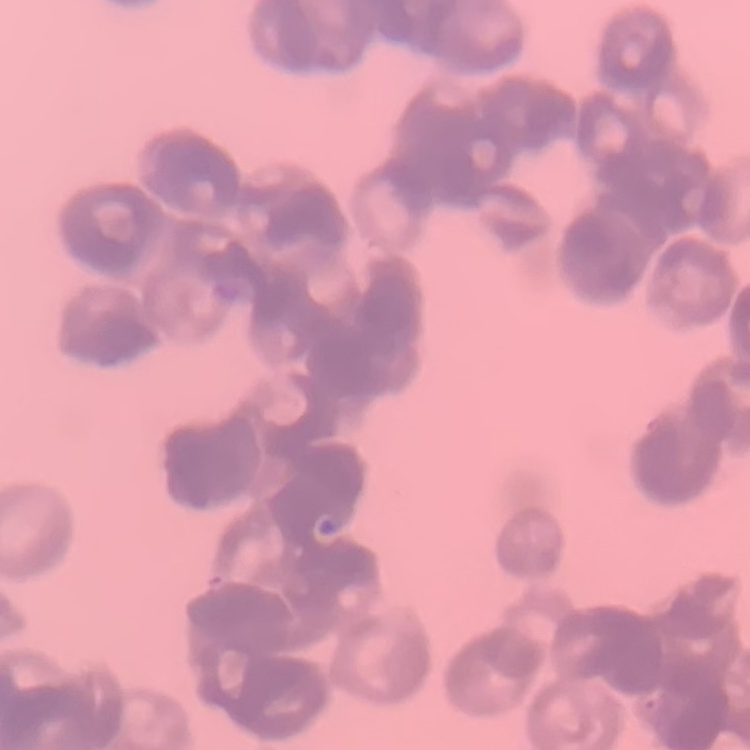

erythrocyte_morphology: rouleaux formation
preparation: thin peripheral smear
image_type: one tile cut from a larger photomicrograph
stain: Field's or Giemsa